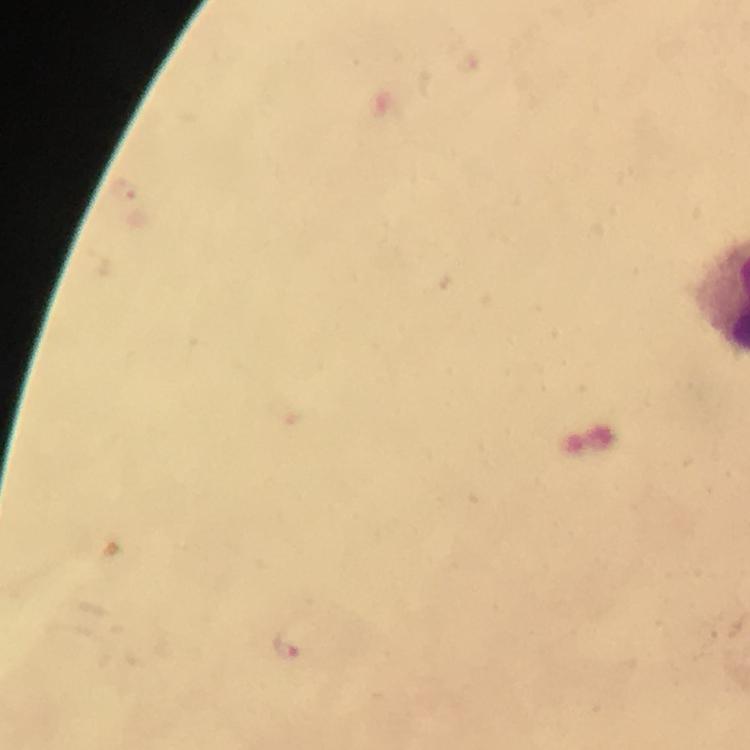
Approximate centers as (x, y) in pixels.
Summary:
  - Malaria parasite locations: (286, 645)
  - Preparation: thick smear
  - Capture: smartphone photograph through a microscope
  - Cropped from: a single field of view
  - Context: from a diagnostic examination for malaria
  - Image size: 750×750 pixels
  - Magnification: 100x
  - Immersion oil: applied
  - Stain: Giemsa